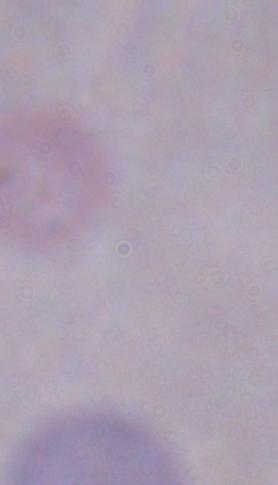

modality = photomicrograph
identification = trypanosome
magnification = 1000x